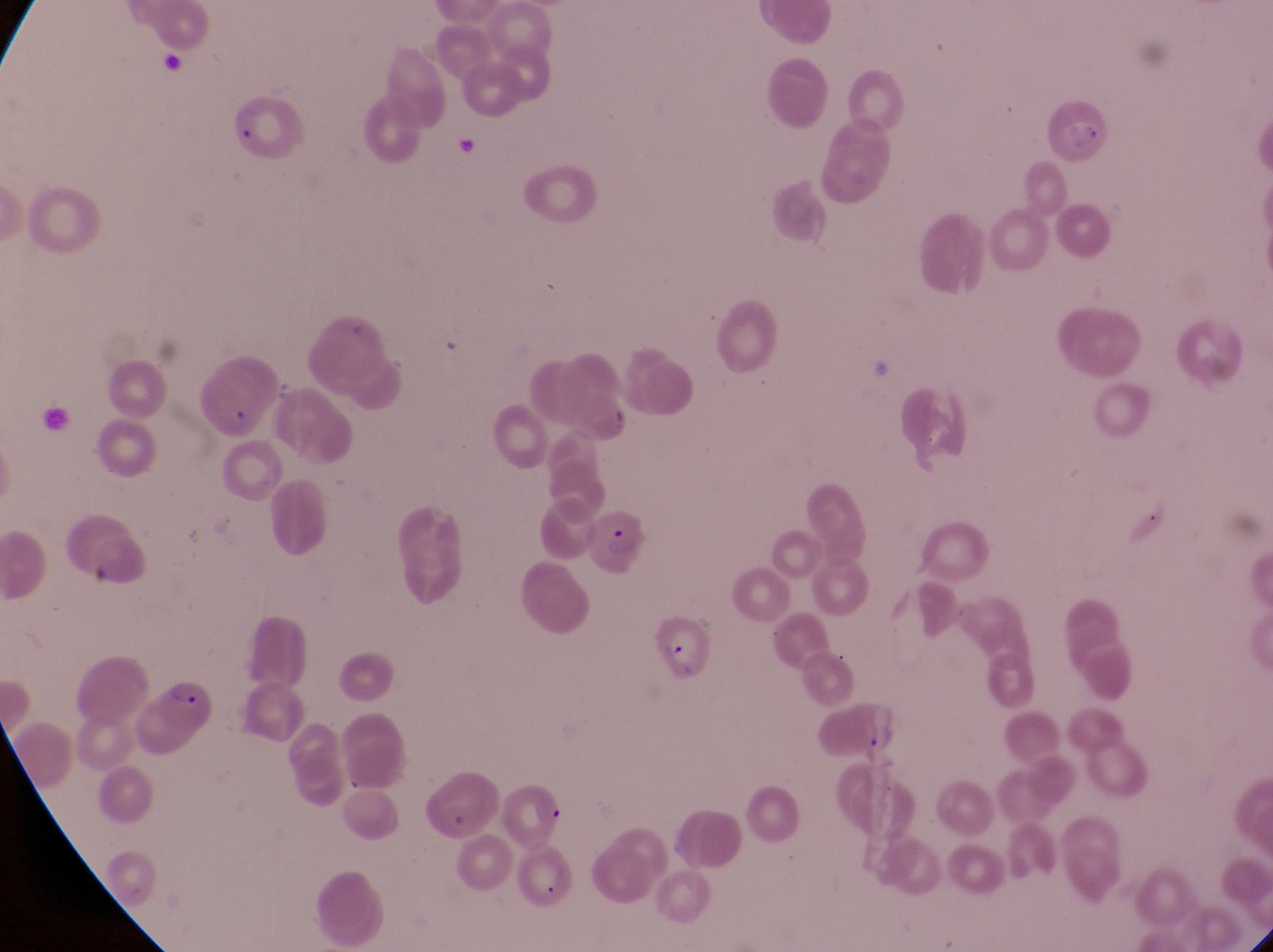
capture = smartphone photograph through the eyepiece of an Olympus CX-23 microscope
preparation = thin blood smear
parasitised red blood cell locations = approximate bounding boxes as {left, top, right, bottom} in pixels: {229, 97, 301, 159}, {587, 497, 649, 574}, {647, 610, 712, 673}, {143, 672, 221, 739}, {499, 772, 569, 844}
trophozoite locations = approximate bounding boxes as {left, top, right, bottom} in pixels: {864, 722, 901, 761}
country = Uganda
magnification = 1000x
image size = 1273×952 pixels
field of view = single